Classify the preparation.
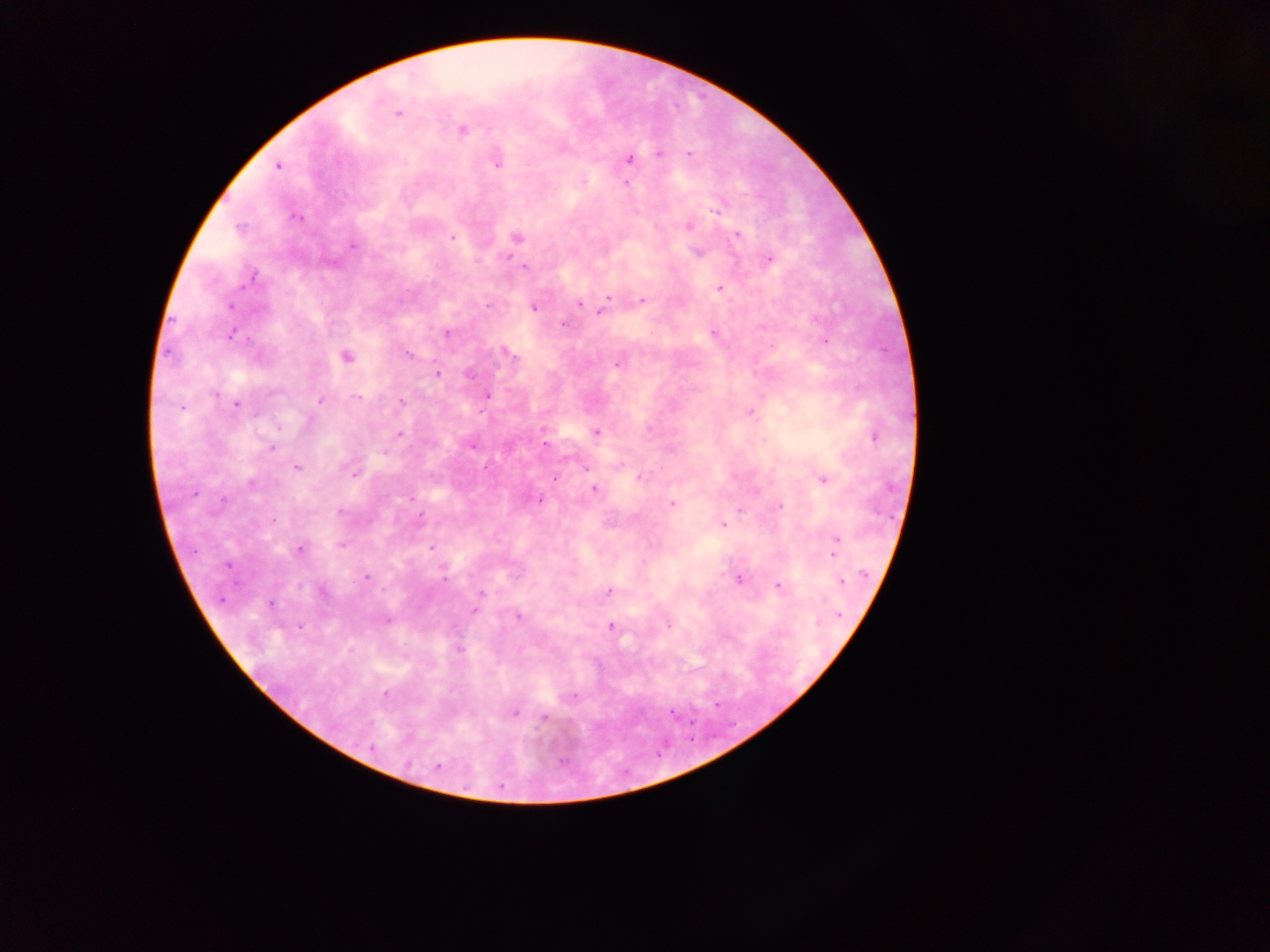

This is a thick smear.

Approximate centers as (x, y) in pixels.
Summary:
  - Malaria parasite locations: (398, 114), (462, 129), (659, 153), (689, 153), (628, 158), (497, 160), (279, 166), (297, 216), (688, 225), (737, 234), (452, 237), (516, 237), (352, 245), (698, 251), (767, 259), (524, 265), (250, 276), (719, 288), (607, 296), (642, 300), (580, 302), (533, 306), (602, 312), (447, 332), (714, 332), (505, 351), (408, 354), (346, 357), (618, 361), (436, 374), (486, 395), (320, 401), (400, 401), (236, 404), (181, 406), (749, 411), (596, 431), (400, 435), (874, 436), (544, 443), (471, 444), (271, 449), (296, 466), (354, 473), (639, 476), (553, 479), (821, 479), (594, 488), (539, 499), (671, 503), (779, 505), (740, 510), (419, 518), (724, 524), (836, 538), (300, 548), (431, 548), (833, 553), (365, 578), (738, 579), (841, 581), (778, 585), (322, 590), (609, 591), (480, 593), (270, 604), (475, 611), (517, 615), (385, 620), (610, 626), (459, 648), (384, 693), (513, 712), (544, 718), (437, 766)
  - Country: Ghana
  - Image size: 1270×952 pixels
  - Capture: mobile-phone photograph through a microscope
  - Field of view: single